Outline every leukocyte.
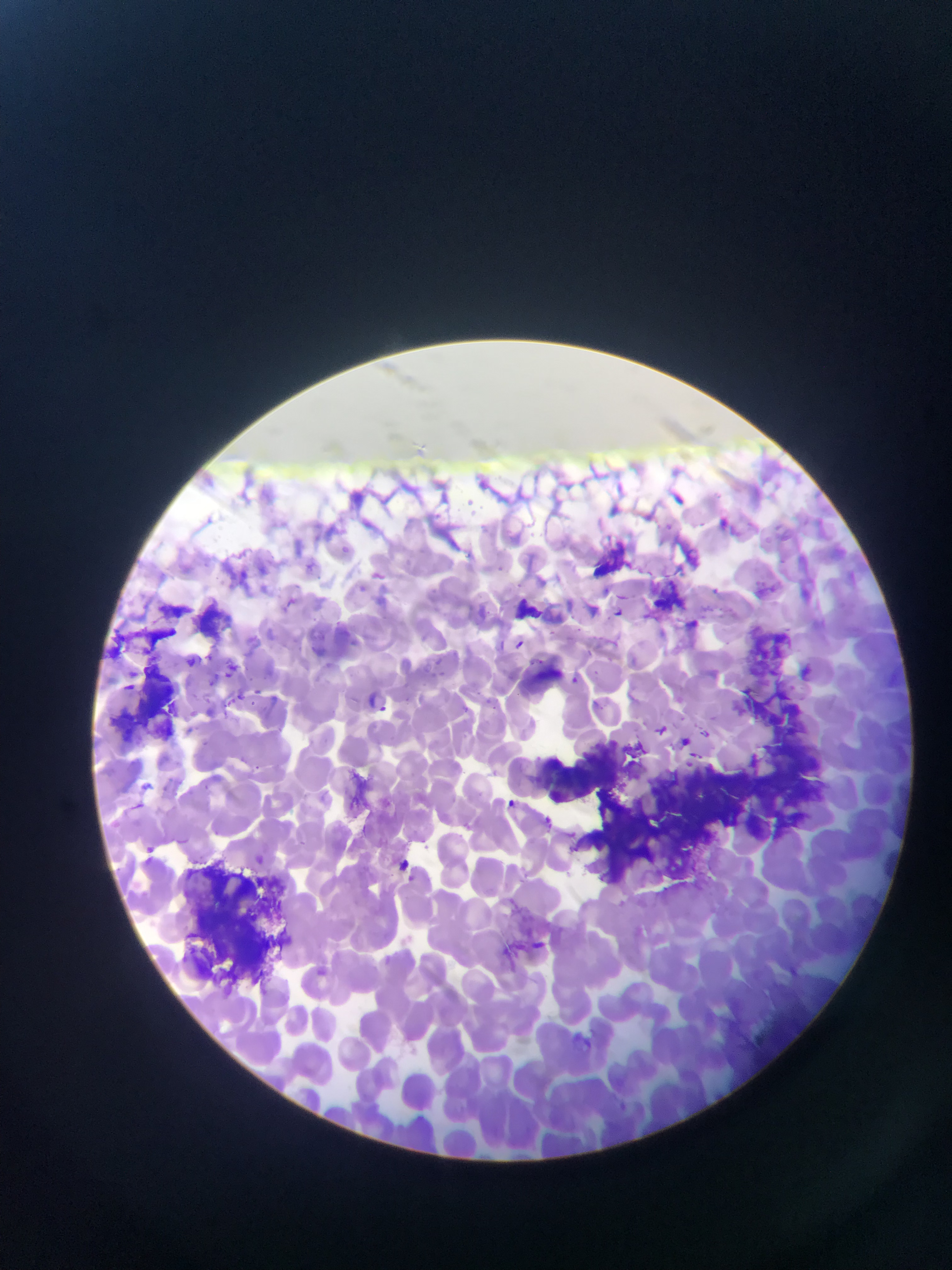
No leukocytes observed.

Approximate bounding boxes as left top right bottom in pixels. Artifact (stain precipitate or debris) locations: 741 621 812 700; 119 660 185 741; 731 686 831 767; 539 740 627 801; 652 758 746 853; 732 759 826 848; 590 783 674 893; 179 860 291 986. Plasmodium parasite locations: 711 584 720 599; 608 606 633 626; 515 638 526 649; 569 665 586 683; 224 666 236 678; 256 683 274 695; 366 688 378 709; 661 725 670 738; 700 726 712 749; 140 774 153 788; 505 798 518 812; 543 815 553 828; 144 835 161 855; 397 856 418 875. Sample from Ghana. Mobile-phone photograph taken through the microscope. Single field of view. Image is 952×1270 pixels. Thin blood film.